Give the extent of all uninfected red blood cells.
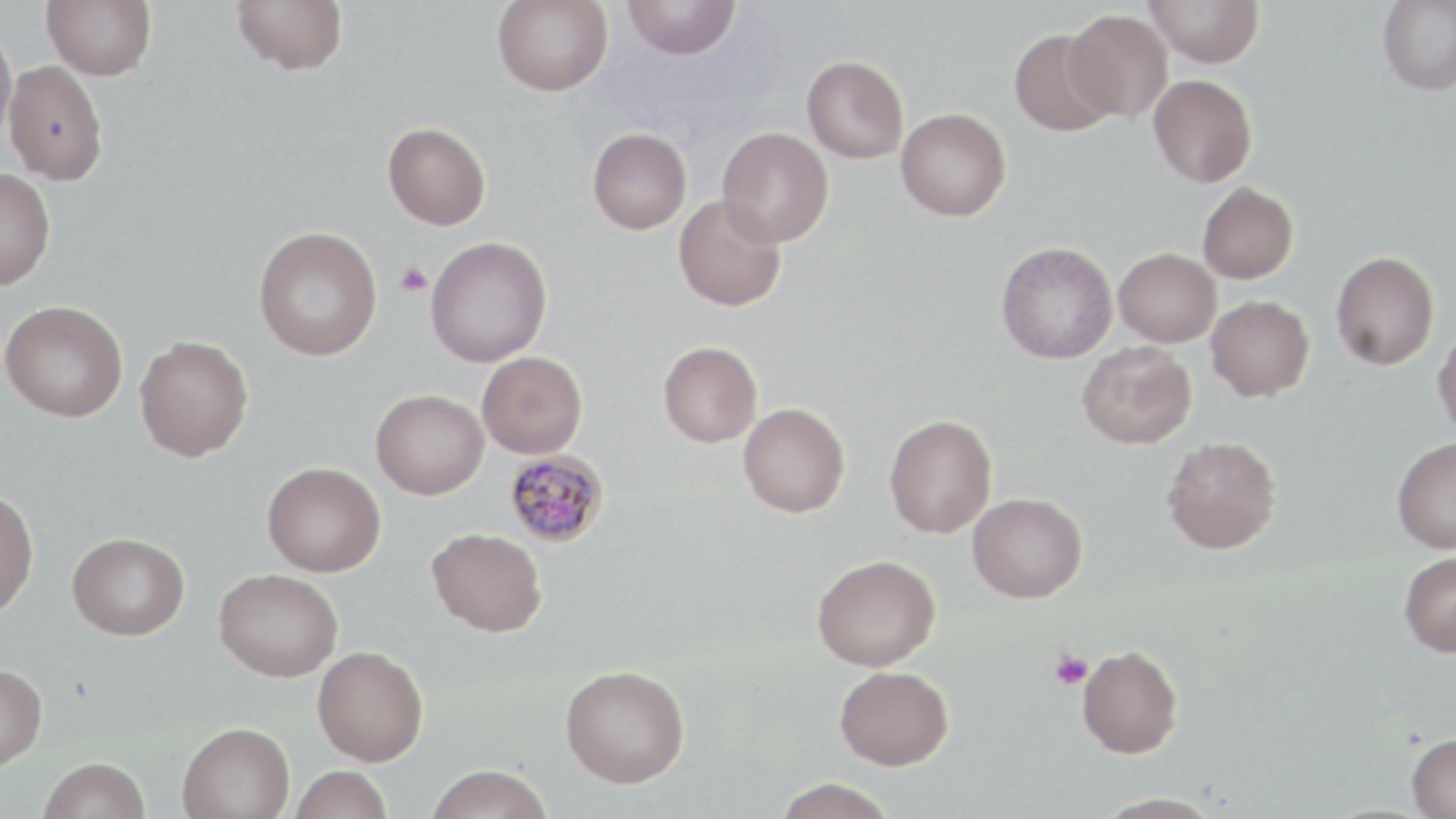
Approximate bounding boxes as (x1, y1, x2, y2) in pixels.
Uninfected red blood cells: (42, 0, 157, 81), (231, 0, 348, 75), (492, 0, 613, 97), (622, 0, 741, 60), (1144, 0, 1264, 68), (1377, 0, 1456, 96), (1064, 9, 1173, 123), (0, 22, 17, 146), (1009, 27, 1117, 136), (802, 56, 908, 164), (3, 61, 108, 185), (1148, 73, 1257, 187), (896, 108, 1011, 221), (383, 122, 491, 230), (717, 126, 834, 247), (587, 127, 692, 234), (0, 168, 56, 291), (1197, 182, 1299, 284), (673, 194, 787, 312), (253, 226, 382, 361), (425, 236, 552, 367), (996, 241, 1118, 364), (1114, 248, 1221, 348), (1330, 251, 1439, 370), (1206, 295, 1314, 401), (1, 300, 128, 422), (1432, 325, 1456, 441), (134, 335, 253, 462), (658, 341, 762, 448), (1077, 342, 1196, 449), (477, 351, 587, 458), (371, 389, 489, 499), (738, 402, 850, 517), (884, 415, 997, 538), (1161, 436, 1281, 554), (1391, 436, 1456, 553), (262, 461, 385, 577), (0, 489, 39, 618), (968, 492, 1087, 603), (427, 527, 547, 636), (67, 532, 189, 640), (1398, 552, 1456, 657), (811, 554, 941, 671), (214, 569, 343, 682), (1077, 644, 1183, 758), (313, 645, 429, 765), (0, 663, 47, 770), (560, 664, 690, 787), (835, 665, 954, 770), (176, 721, 295, 819), (1406, 733, 1456, 819), (38, 757, 151, 819), (425, 764, 553, 819), (290, 765, 393, 819), (773, 778, 898, 819), (1090, 792, 1228, 819).

Summary:
  - Platelet locations: (395, 260, 433, 297), (1049, 648, 1093, 690)
  - Plasmodium malariae-infected red blood cell locations: (504, 450, 610, 547)
  - Slide-level diagnosis: Plasmodium malariae
  - Image size: 1456×819 pixels
  - Magnification: 1000x
  - Field of view: one of a larger specimen
  - Preparation: thin blood smear
  - Stain: May-Grünwald-Giemsa
  - Modality: optical microscopy